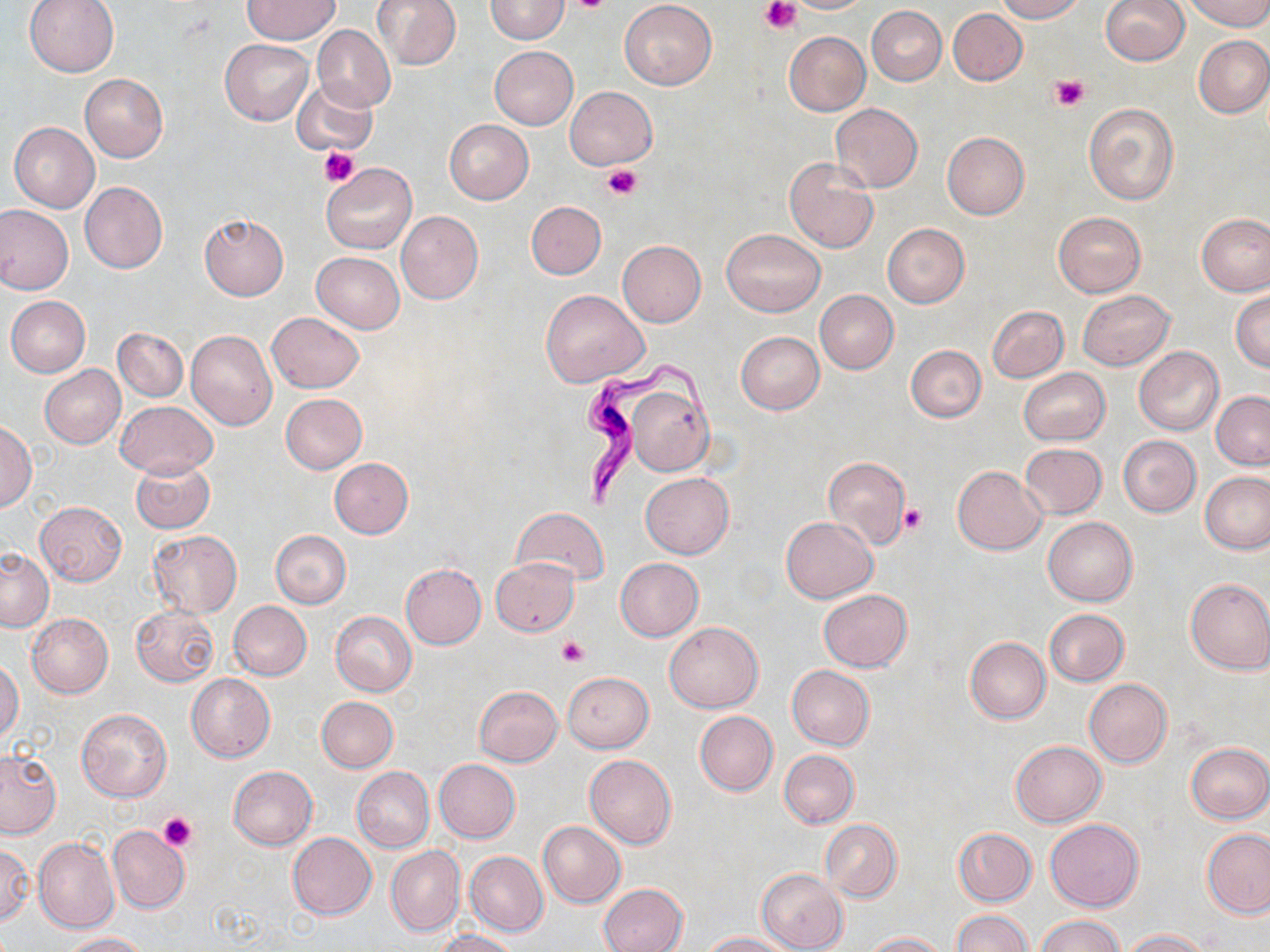
slide_level_diagnosis: Trypanosoma brucei
uninfected_red_blood_cell_locations: 'approximate bounding boxes as (x1, y1, x2, y2) in pixels: (24, 0, 120, 77), (242, 0, 339, 43), (374, 0, 461, 70), (484, 0, 570, 43), (621, 0, 717, 89), (785, 0, 873, 14), (994, 0, 1086, 22), (1184, 0, 1270, 30), (1100, 1, 1188, 66), (867, 5, 947, 85), (948, 8, 1027, 85), (311, 24, 395, 112), (784, 31, 871, 117), (1194, 35, 1270, 118), (220, 39, 314, 125), (490, 46, 578, 129), (80, 74, 167, 162), (294, 78, 379, 155), (565, 85, 658, 169), (1083, 102, 1181, 205), (830, 103, 922, 192), (444, 120, 533, 203), (8, 122, 99, 213), (942, 132, 1029, 219), (784, 157, 879, 252), (321, 162, 417, 255), (80, 181, 168, 274), (526, 201, 605, 279), (0, 205, 73, 294), (396, 210, 484, 305), (1053, 211, 1146, 296), (199, 213, 288, 300), (1197, 214, 1270, 296), (882, 223, 969, 308), (720, 229, 825, 316), (617, 240, 706, 326), (311, 251, 405, 332), (541, 289, 649, 387), (815, 289, 898, 374), (1078, 290, 1175, 370), (1231, 290, 1270, 372), (5, 295, 91, 377), (986, 306, 1068, 382), (266, 311, 365, 393), (113, 327, 187, 402), (185, 330, 277, 430), (736, 332, 825, 415), (907, 345, 986, 422), (1134, 346, 1224, 435), (40, 365, 126, 449), (1018, 368, 1111, 446), (625, 386, 712, 475), (1212, 392, 1270, 470), (280, 393, 367, 473), (116, 400, 217, 478), (1, 422, 37, 512), (1118, 435, 1201, 516), (1019, 442, 1107, 519), (821, 457, 910, 549), (329, 458, 413, 538), (130, 459, 215, 534), (953, 466, 1047, 554), (1200, 471, 1269, 553), (640, 472, 733, 558), (36, 501, 126, 584), (511, 506, 610, 587), (782, 517, 877, 603), (1043, 517, 1137, 605), (147, 530, 243, 618), (271, 530, 352, 608), (1, 548, 54, 631), (492, 558, 579, 635), (615, 558, 704, 641), (401, 563, 486, 649), (1184, 577, 1270, 675), (818, 589, 912, 672), (228, 600, 312, 680), (130, 605, 219, 687), (1044, 609, 1129, 686), (330, 611, 417, 696), (27, 613, 114, 698), (664, 622, 762, 712), (964, 637, 1050, 724), (0, 660, 24, 742), (786, 665, 874, 750), (562, 671, 653, 753), (186, 674, 275, 762), (1084, 678, 1173, 768), (474, 686, 563, 766), (316, 696, 398, 772), (75, 709, 171, 803), (695, 710, 778, 796), (1011, 740, 1106, 826), (1186, 742, 1269, 824), (0, 748, 62, 838), (779, 749, 859, 828), (584, 754, 677, 849), (434, 759, 521, 843), (228, 766, 317, 850), (352, 767, 435, 852), (1045, 818, 1144, 911), (820, 819, 901, 902), (538, 821, 625, 907), (107, 825, 189, 913), (953, 828, 1036, 906), (1202, 829, 1270, 918), (288, 832, 377, 920), (33, 837, 118, 933), (0, 843, 33, 925), (386, 846, 464, 936), (464, 850, 548, 936), (756, 867, 848, 952), (599, 883, 688, 952), (952, 910, 1031, 952), (1037, 916, 1122, 952), (431, 928, 518, 951), (1121, 928, 1213, 952), (60, 931, 147, 951), (864, 931, 950, 951), (704, 933, 794, 952)'
field_of_view: single
trypanosoma_brucei_locations: 'approximate bounding boxes as (x1, y1, x2, y2) in pixels: (579, 356, 717, 506)'
magnification: 1000x
stain: May-Grünwald-Giemsa
preparation: thin blood smear
platelet_locations: 'approximate bounding boxes as (x1, y1, x2, y2) in pixels: (564, 0, 611, 14), (760, 0, 801, 37), (1051, 75, 1088, 111), (320, 146, 357, 187), (602, 165, 643, 201), (900, 504, 927, 534), (556, 636, 590, 668), (157, 813, 196, 852)'
modality: optical microscopy
image_size: 1270×952 pixels